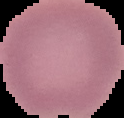 From a thin blood film. Result: no Plasmodium parasites seen. Image is 124×118 pixels. The area outside the segmented cell region is set to black.